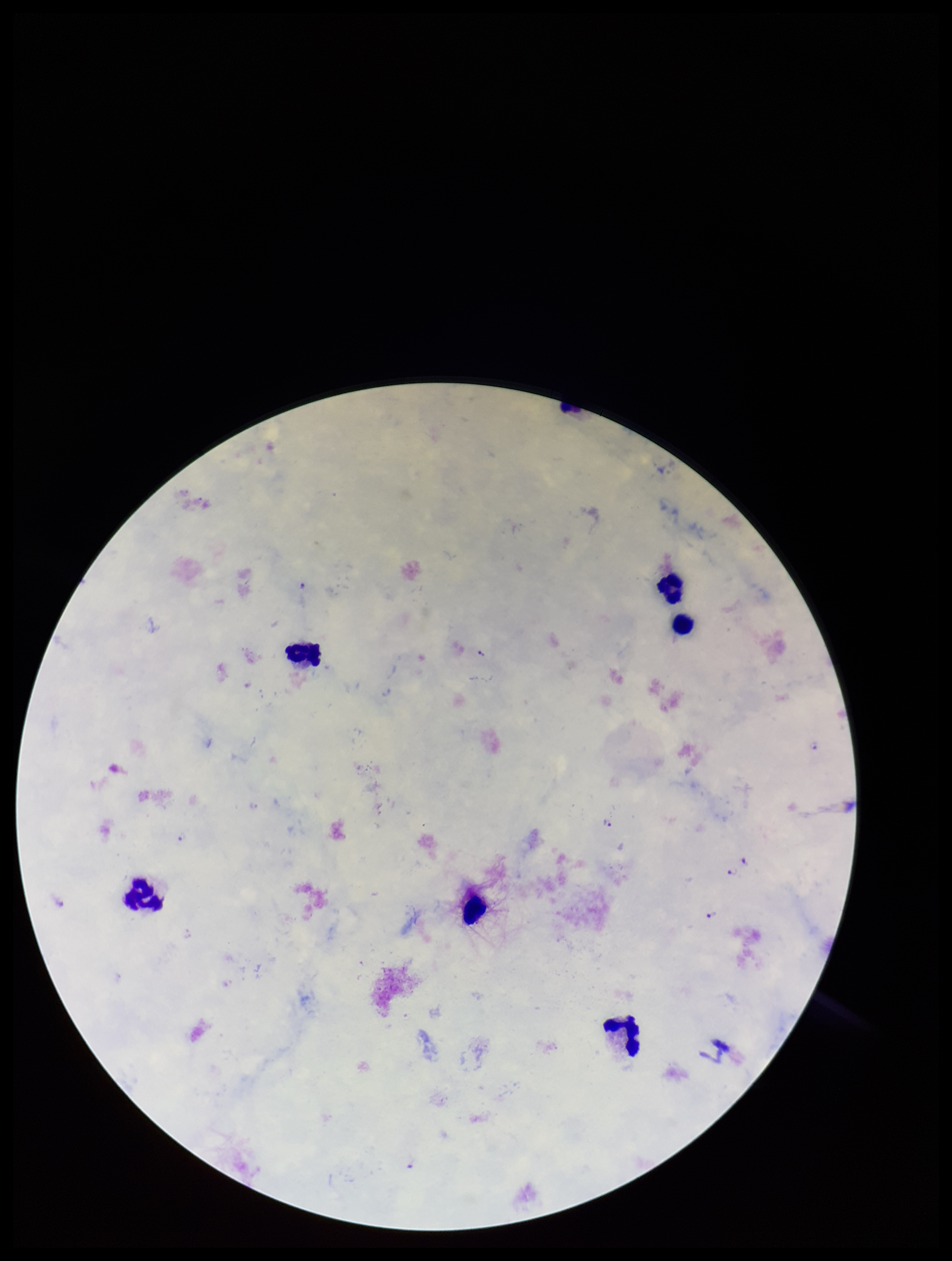
capture = smartphone photograph through the microscope eyepiece
patient malaria status = positive
leukocyte count = 6
species reported for this patient = Plasmodium falciparum
preparation = thick
image size = 952×1261 pixels
parasite count = 6
Plasmodium parasites = identified
field of view = one from this slide
stain = Giemsa